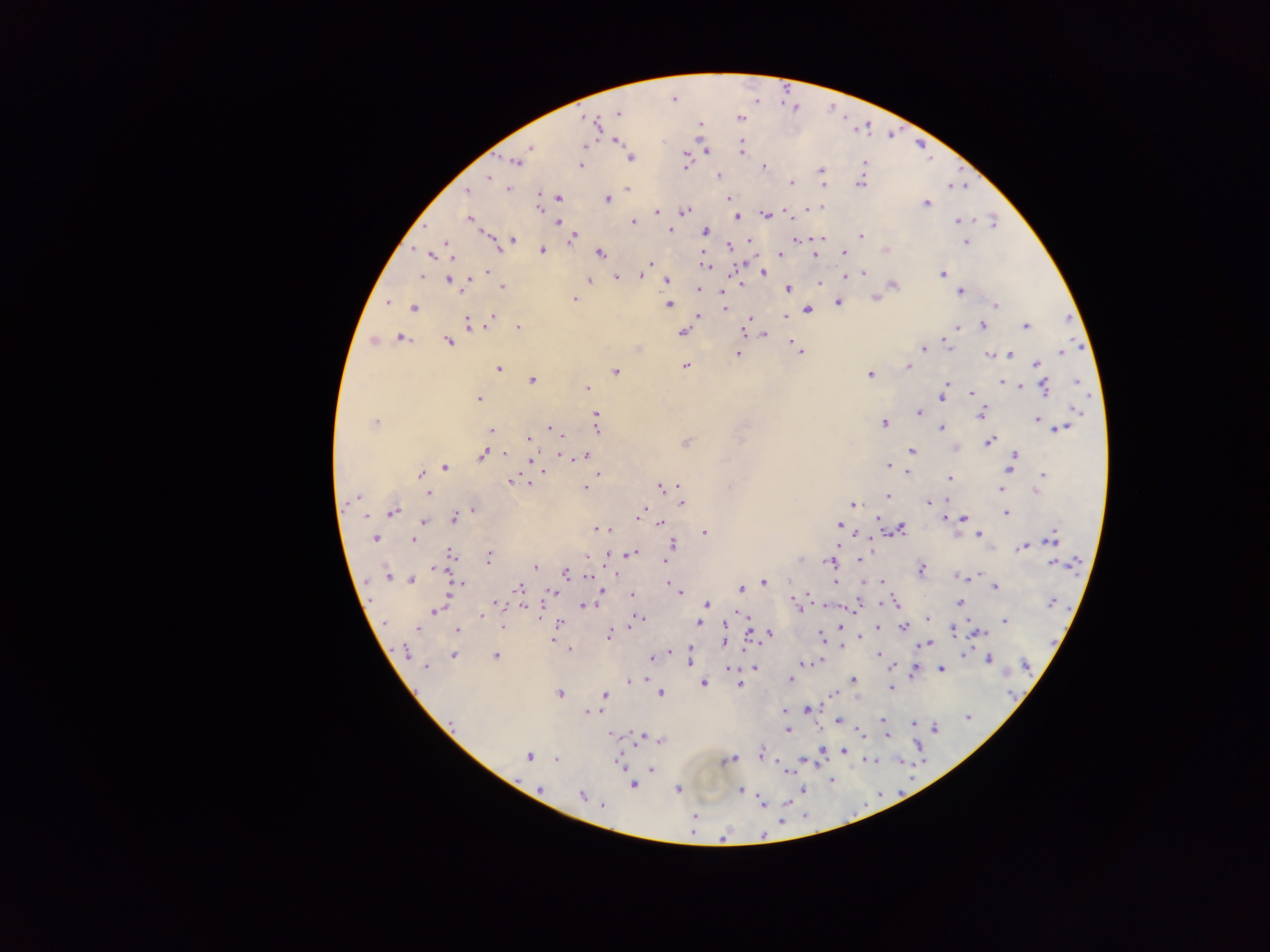
image_size: 1270×952 pixels
plasmodium_parasite_locations: 'approximate centers as (x, y) in pixels: (673, 100), (618, 113), (739, 118), (588, 120), (595, 124), (700, 125), (615, 141), (584, 146), (530, 148), (741, 149), (706, 150), (631, 159), (515, 161), (865, 162), (581, 165), (685, 166), (764, 167), (821, 169), (718, 175), (488, 177), (792, 182), (860, 183), (823, 185), (627, 188), (508, 189), (467, 191), (559, 198), (728, 198), (607, 199), (926, 204), (539, 207), (819, 208), (786, 211), (657, 212), (684, 212), (764, 215), (736, 217), (469, 220), (957, 221), (558, 222), (993, 222), (633, 223), (669, 229), (705, 231), (861, 236), (573, 238), (820, 238), (512, 240), (796, 240), (750, 241), (966, 242), (448, 243), (729, 246), (886, 249), (543, 251), (600, 253), (844, 253), (780, 254), (432, 255), (814, 255), (650, 263), (705, 263), (487, 272), (764, 273), (863, 273), (942, 273), (642, 275), (421, 276), (617, 277), (589, 280), (667, 280), (450, 282), (820, 283), (893, 285), (502, 286), (464, 288), (788, 288), (699, 289), (960, 292), (573, 299), (876, 299), (388, 303), (838, 303), (669, 305), (996, 305), (413, 308), (724, 308), (808, 309), (698, 315), (785, 316), (493, 317), (749, 319), (468, 324), (982, 325), (957, 326), (1026, 326), (518, 327), (746, 329), (683, 333), (765, 334), (401, 338), (449, 342), (947, 343), (793, 344), (924, 349), (798, 350), (1061, 353), (737, 354), (989, 355), (1009, 355), (1036, 364), (685, 365), (909, 367), (499, 368), (616, 371), (870, 374), (532, 381), (1076, 382), (1003, 383), (946, 384), (1020, 386), (587, 388), (1045, 388), (972, 394), (943, 397), (478, 399), (1076, 410), (981, 412), (918, 413), (596, 415), (1037, 419), (375, 422), (883, 423), (597, 427), (550, 428), (942, 428), (1061, 429), (491, 430), (555, 432), (528, 439), (989, 442), (686, 444), (912, 451), (504, 454), (483, 455), (1016, 455), (585, 456), (566, 457), (888, 465), (1011, 466), (445, 468), (539, 468), (543, 471), (909, 472), (598, 474), (422, 475), (1043, 475), (950, 478), (512, 481), (528, 481), (678, 486), (586, 487), (661, 487), (1001, 489), (1037, 491), (428, 494), (888, 496), (358, 497), (349, 501), (947, 501), (928, 502), (682, 503), (852, 505), (473, 510), (642, 512), (394, 513), (1006, 513), (366, 516), (878, 518), (944, 518), (964, 518), (453, 519), (423, 522), (660, 523), (839, 526), (902, 529), (598, 530), (704, 533), (980, 535), (375, 538), (414, 540), (1052, 540), (671, 544), (1023, 546), (632, 553), (451, 554), (609, 554), (488, 557), (862, 559), (664, 561), (829, 562), (1054, 564), (535, 567), (921, 569), (565, 573), (387, 576), (590, 576), (961, 576), (968, 577), (412, 580), (765, 582), (835, 582), (883, 582), (460, 583), (454, 587), (996, 587), (520, 588), (741, 589), (676, 591), (602, 592), (553, 593), (680, 593), (631, 595), (894, 601), (497, 603), (960, 603), (1052, 603), (706, 605), (799, 605), (583, 606), (434, 611), (481, 615), (928, 618), (638, 619), (1005, 621), (635, 622), (559, 623), (699, 623), (385, 624), (418, 627), (502, 627), (841, 627), (878, 627), (904, 627), (457, 629), (953, 631), (979, 633), (769, 634), (609, 635), (822, 636), (861, 637), (552, 640), (725, 641), (926, 644), (569, 649), (405, 651), (670, 651), (690, 651), (878, 654), (964, 654), (453, 655), (495, 656), (652, 658), (989, 659), (820, 660), (689, 661), (804, 663), (1025, 665), (426, 667), (753, 668), (729, 669), (941, 669), (915, 671), (790, 680), (854, 680), (630, 681), (703, 683), (739, 684), (890, 688), (834, 693), (559, 694), (605, 694), (661, 694), (807, 708), (784, 711), (588, 712), (968, 718), (883, 719), (839, 721), (914, 723), (936, 727), (788, 731), (859, 732), (611, 735), (887, 735), (641, 736), (661, 740), (823, 749), (844, 751), (761, 753), (528, 756), (556, 760), (728, 760), (803, 760), (870, 761), (619, 762), (651, 770), (832, 781), (632, 785), (539, 788), (678, 790), (804, 790), (741, 791), (582, 795), (762, 804), (602, 806), (695, 817), (781, 822), (764, 834), (723, 838)'
capture: mobile-phone photograph through a microscope
country: Ghana
field_of_view: single
preparation: thick blood smear